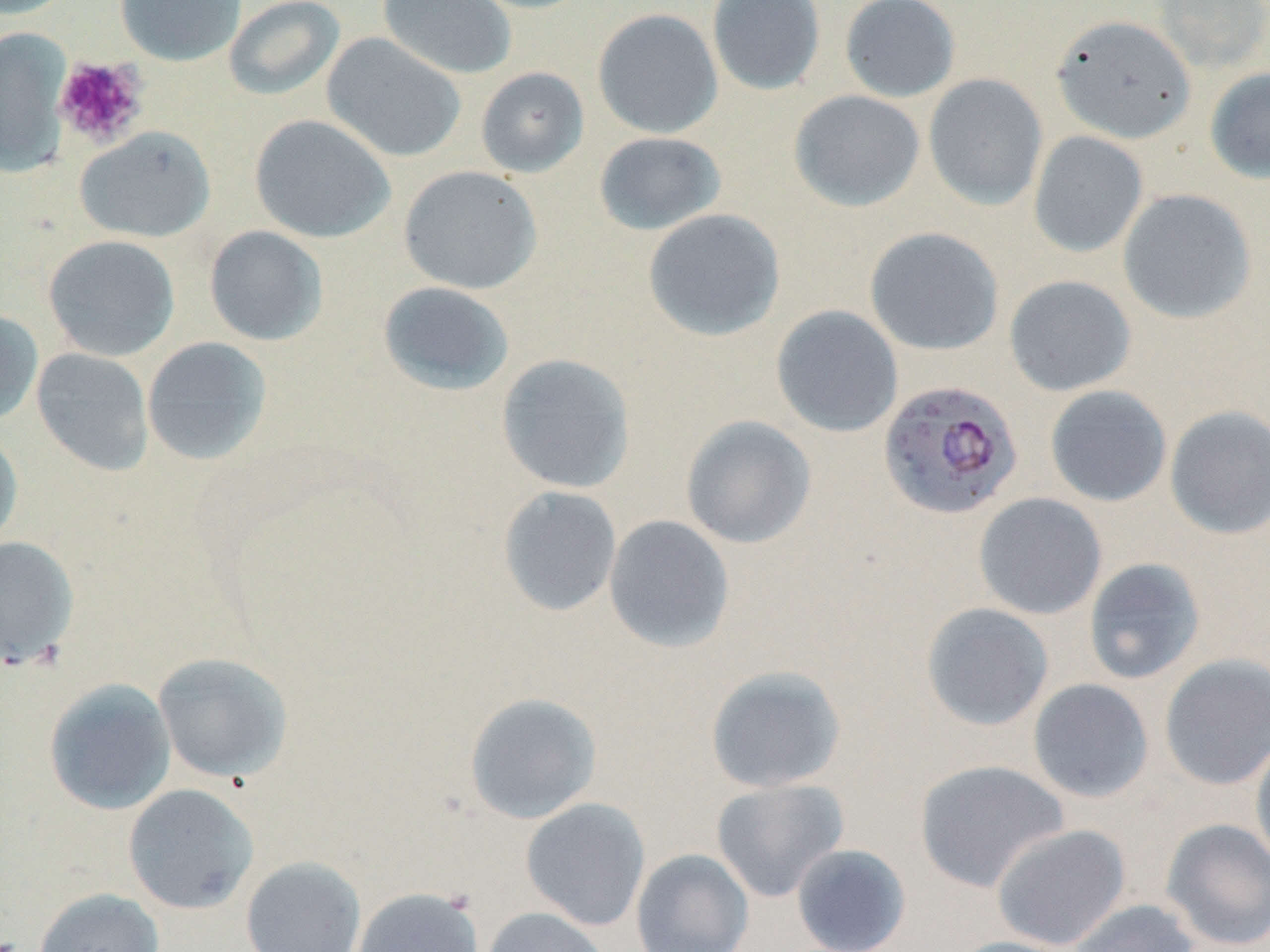

Approximate bounding boxes as (x1,y1)-(x2,y2) corner pairs in pixels. Platelet locations: (52,55)-(148,147). Uninfected red blood cell locations: (0,0)-(75,20), (114,0)-(247,66), (223,0)-(346,101), (377,0)-(517,80), (460,0)-(597,14), (706,0)-(826,95), (840,0)-(961,103), (1153,0)-(1270,73), (592,8)-(723,139), (1051,14)-(1195,143), (0,27)-(72,177), (321,32)-(467,163), (475,67)-(589,178), (1204,68)-(1270,184), (923,74)-(1048,210), (789,89)-(926,212), (249,114)-(395,243), (74,126)-(216,243), (593,131)-(727,236), (1028,131)-(1148,258), (398,165)-(543,294), (1117,188)-(1257,325), (642,208)-(786,342), (204,226)-(328,346), (864,227)-(1004,355), (43,234)-(180,361), (1004,275)-(1136,396), (378,281)-(515,396), (771,305)-(904,437), (0,308)-(43,426), (141,336)-(273,466), (32,348)-(154,476), (496,353)-(636,493), (1044,385)-(1172,507), (1165,405)-(1270,540), (681,415)-(817,549), (0,427)-(23,552), (497,486)-(622,617), (973,492)-(1107,620), (603,514)-(735,653), (0,536)-(79,670), (1083,558)-(1206,685), (920,602)-(1054,731), (153,652)-(293,783), (1159,653)-(1270,791), (704,664)-(847,793), (43,678)-(177,815), (1027,678)-(1154,803), (464,692)-(602,824), (1250,733)-(1270,872), (913,759)-(1070,893), (711,778)-(850,902), (122,783)-(259,914), (520,797)-(651,931), (1160,818)-(1270,951), (991,823)-(1131,950), (791,843)-(912,952), (631,848)-(755,952), (241,856)-(366,952), (33,887)-(164,952), (353,887)-(483,951), (1065,898)-(1202,952), (480,906)-(612,952), (947,936)-(1080,952). Plasmodium falciparum-infected red blood cell locations: (877,379)-(1024,520). Slide-level diagnosis: Plasmodium falciparum. Captured at 1000x magnification. Image is 1270×952 pixels. Light microscopy. Single field of view. Thin blood film. May-Grünwald-Giemsa stain.